Give the position of every malaria parasite.
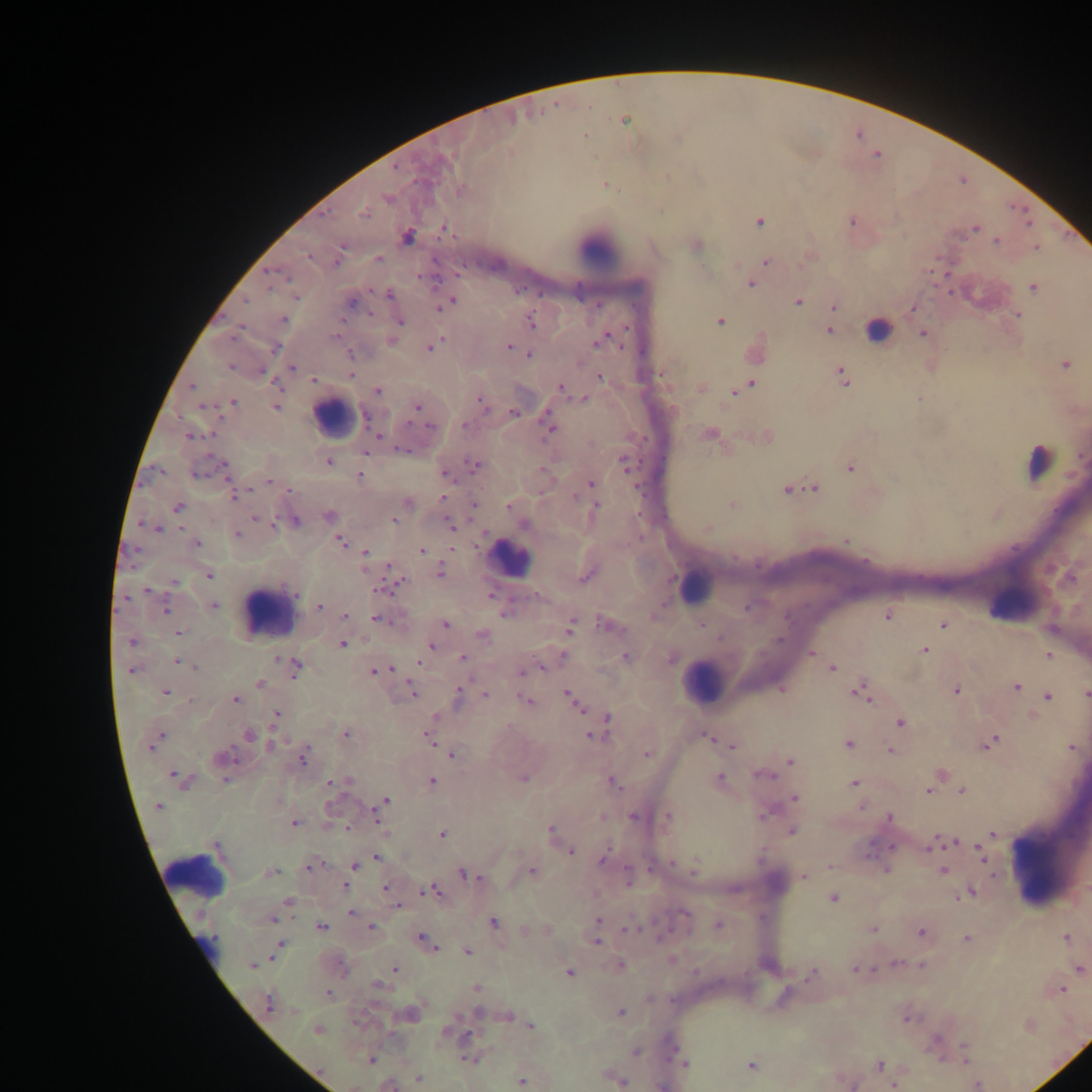
Approximate centers as {x, y} in pixels.
Malaria parasites: {624, 120}, {585, 135}, {395, 168}, {667, 177}, {606, 185}, {461, 189}, {387, 198}, {364, 214}, {851, 221}, {760, 222}, {1028, 222}, {976, 227}, {444, 230}, {407, 236}, {997, 240}, {342, 247}, {1037, 247}, {308, 256}, {378, 258}, {338, 262}, {767, 262}, {270, 272}, {287, 277}, {751, 285}, {1033, 287}, {388, 295}, {450, 301}, {246, 302}, {351, 302}, {798, 302}, {834, 307}, {913, 308}, {1018, 314}, {283, 319}, {400, 321}, {530, 322}, {719, 322}, {829, 331}, {923, 334}, {335, 335}, {605, 340}, {392, 341}, {597, 342}, {431, 347}, {509, 347}, {275, 348}, {351, 355}, {530, 355}, {1065, 365}, {230, 368}, {292, 368}, {351, 375}, {600, 377}, {844, 378}, {313, 380}, {275, 384}, {751, 385}, {192, 387}, {561, 388}, {378, 391}, {735, 392}, {582, 399}, {482, 402}, {234, 403}, {276, 407}, {417, 407}, {514, 413}, {464, 425}, {430, 427}, {549, 428}, {377, 436}, {189, 437}, {403, 450}, {365, 452}, {1081, 457}, {329, 462}, {623, 462}, {223, 465}, {475, 465}, {851, 467}, {198, 473}, {445, 475}, {360, 476}, {270, 482}, {591, 483}, {814, 488}, {290, 489}, {786, 490}, {234, 496}, {443, 498}, {575, 498}, {408, 503}, {474, 505}, {732, 505}, {509, 506}, {597, 506}, {178, 507}, {329, 515}, {256, 519}, {394, 520}, {296, 521}, {450, 524}, {524, 525}, {707, 527}, {158, 529}, {237, 534}, {341, 541}, {846, 541}, {196, 543}, {421, 550}, {366, 553}, {389, 569}, {441, 573}, {209, 574}, {587, 576}, {174, 582}, {147, 590}, {381, 590}, {295, 594}, {127, 599}, {214, 606}, {319, 607}, {746, 608}, {166, 611}, {504, 614}, {345, 616}, {888, 617}, {376, 619}, {446, 623}, {604, 625}, {702, 625}, {943, 625}, {571, 626}, {178, 633}, {483, 636}, {131, 642}, {343, 644}, {431, 645}, {924, 650}, {811, 653}, {1048, 655}, {564, 656}, {626, 656}, {462, 658}, {276, 659}, {177, 662}, {418, 663}, {295, 666}, {197, 667}, {542, 668}, {832, 668}, {390, 669}, {132, 670}, {374, 671}, {523, 672}, {260, 684}, {1016, 687}, {957, 690}, {413, 691}, {166, 692}, {863, 692}, {1086, 693}, {485, 695}, {570, 695}, {457, 696}, {1048, 696}, {236, 700}, {575, 701}, {527, 702}, {277, 714}, {434, 718}, {607, 720}, {901, 723}, {347, 735}, {249, 736}, {593, 736}, {709, 737}, {430, 738}, {158, 739}, {991, 743}, {848, 744}, {153, 745}, {272, 745}, {733, 746}, {1072, 747}, {891, 750}, {646, 754}, {453, 755}, {224, 757}, {304, 758}, {791, 761}, {764, 775}, {176, 776}, {719, 778}, {182, 779}, {523, 779}, {225, 780}, {432, 781}, {612, 782}, {330, 784}, {854, 784}, {928, 790}, {962, 791}, {794, 798}, {385, 801}, {158, 806}, {862, 808}, {765, 813}, {635, 816}, {667, 816}, {377, 817}, {889, 818}, {294, 823}, {551, 830}, {792, 831}, {993, 833}, {442, 834}, {956, 841}, {216, 846}, {931, 846}, {979, 847}, {572, 851}, {981, 855}, {377, 857}, {604, 860}, {672, 863}, {311, 866}, {355, 866}, {831, 866}, {695, 869}, {886, 870}, {945, 870}, {270, 872}, {532, 872}, {463, 874}, {804, 877}, {344, 886}, {385, 887}, {431, 891}, {972, 893}, {834, 899}, {288, 901}, {399, 906}, {352, 913}, {686, 913}, {273, 920}, {599, 921}, {494, 922}, {718, 925}, {321, 927}, {370, 928}, {630, 929}, {873, 929}, {524, 930}, {920, 932}, {1066, 937}, {422, 939}, {966, 939}, {596, 943}, {281, 944}, {429, 945}, {467, 951}, {896, 963}, {252, 965}, {620, 965}, {922, 965}, {1080, 969}, {395, 970}, {855, 970}, {570, 973}, {813, 973}, {379, 985}, {476, 988}, {1062, 990}, {329, 994}, {268, 1003}, {620, 1012}, {478, 1013}, {508, 1016}, {908, 1019}, {531, 1026}, {318, 1030}, {449, 1033}, {936, 1041}, {635, 1052}, {966, 1054}, {371, 1059}, {469, 1059}, {685, 1064}, {752, 1066}, {879, 1066}, {418, 1078}, {522, 1081}, {622, 1081}, {977, 1084}, {390, 1085}, {893, 1085}.

Leukocyte locations: {599, 250}, {878, 328}, {333, 416}, {1039, 461}, {510, 558}, {696, 585}, {1018, 598}, {269, 610}, {702, 681}, {1030, 868}, {194, 875}, {205, 946}. Sample from Ghana. Single field of view. Thick blood smear. Image is 1092×1092 pixels. Photographed through a microscope with a mobile-phone camera.